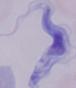

{
  "modality": "micrograph",
  "magnification": "1000x",
  "identification": "trypanosome"
}